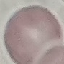
Summary:
  - Result: negative for malaria parasites
  - Stain: Giemsa
  - Capture: smartphone through the microscope eyepiece
  - Image type: cell patch, automatically extracted from a larger field of view and resized to 64 × 64 pixels
  - Preparation: thin blood film